Name the parasite shown.
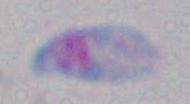

Toxoplasma gondii.

{
  "modality": "micrograph",
  "magnification": "1000x"
}